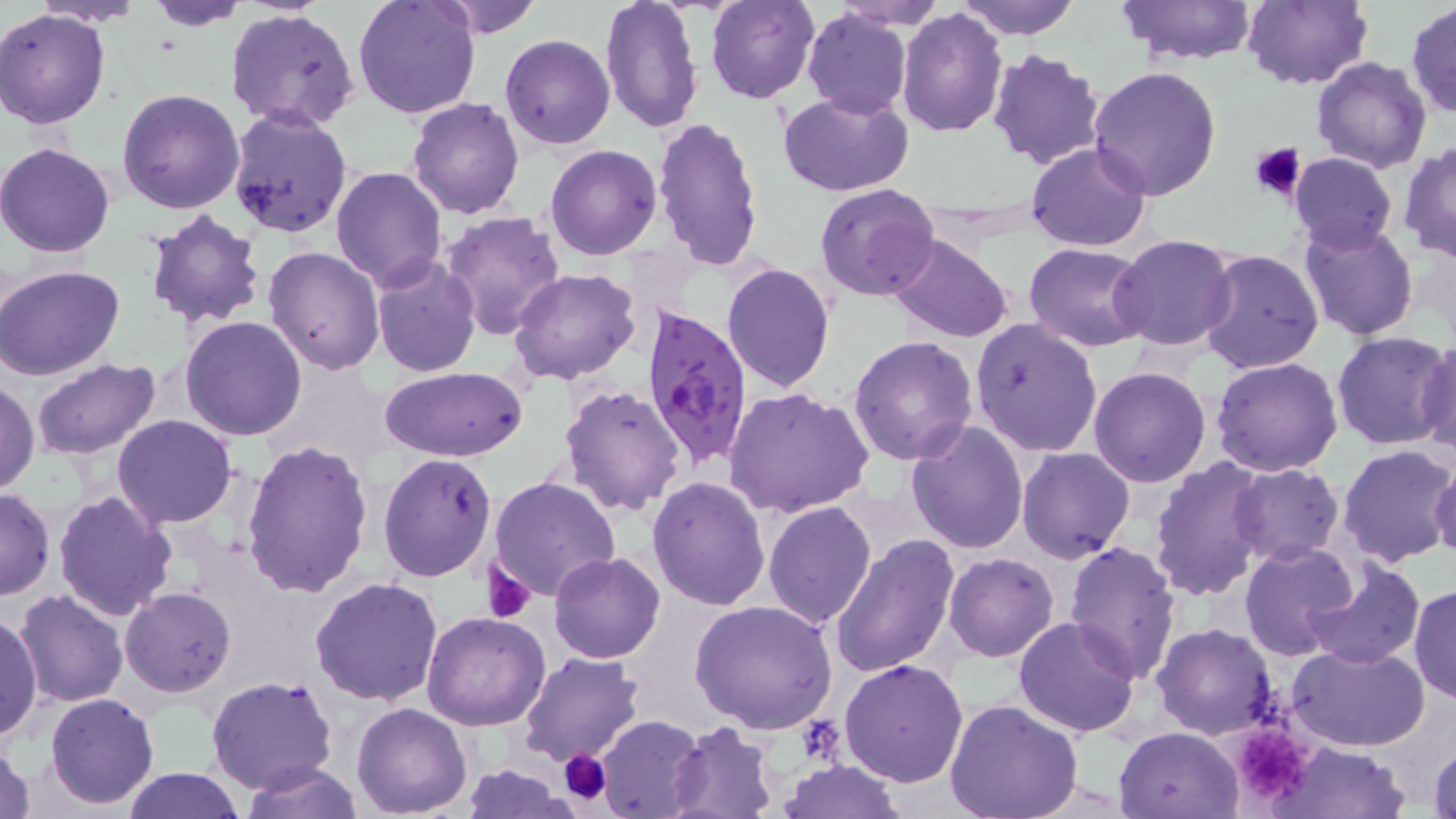

Summary:
  - Coordinate format: approximate bounding boxes as (x1,y1)-(x2,y2) corner pairs in pixels
  - Uninfected red blood cell locations: (140,0)-(250,29), (354,0)-(481,122), (431,0)-(543,40), (598,0)-(704,135), (705,0)-(819,104), (830,0)-(947,31), (953,0)-(1083,40), (1116,0)-(1260,66), (1240,0)-(1371,90), (31,2)-(148,27), (1406,3)-(1455,118), (227,7)-(361,133), (897,7)-(1009,137), (0,9)-(113,128), (802,9)-(913,119), (501,34)-(615,149), (988,49)-(1107,172), (1312,55)-(1431,173), (1087,64)-(1223,200), (779,87)-(916,199), (116,88)-(246,213), (408,98)-(525,220), (227,107)-(353,237), (651,116)-(763,271), (0,141)-(118,257), (1026,141)-(1152,250), (1400,142)-(1456,261), (545,145)-(663,261), (1288,153)-(1398,256), (331,166)-(447,290), (814,184)-(941,302), (143,210)-(267,331), (438,210)-(566,341), (1298,218)-(1420,340), (1110,233)-(1239,351), (888,235)-(1014,343), (1024,241)-(1150,351), (263,245)-(384,375), (1199,248)-(1324,375), (370,255)-(481,376), (722,262)-(836,394), (0,265)-(127,381), (509,269)-(641,385), (181,317)-(307,441), (970,318)-(1103,456), (1331,330)-(1455,449), (849,335)-(980,466), (1415,336)-(1456,459), (1212,357)-(1344,476), (32,359)-(161,458), (382,367)-(529,460), (1089,367)-(1212,487), (1,379)-(39,495), (558,383)-(689,517), (723,384)-(876,520), (113,414)-(237,529), (905,420)-(1031,555), (241,439)-(374,597), (1336,445)-(1456,568), (1017,447)-(1136,564), (377,453)-(497,582), (1148,456)-(1272,601), (1429,458)-(1456,564), (1228,464)-(1344,565), (647,476)-(772,611), (489,477)-(621,603), (0,488)-(54,600), (54,490)-(179,621), (762,499)-(878,629), (830,535)-(959,679), (1064,540)-(1183,683), (1240,541)-(1362,661), (549,551)-(665,663), (943,553)-(1059,662), (1302,555)-(1426,670), (309,575)-(446,707), (1410,582)-(1456,704), (121,587)-(235,696), (14,590)-(129,706), (0,598)-(80,726), (688,600)-(839,733), (1,609)-(44,744), (421,611)-(550,731), (1014,616)-(1142,737), (1152,622)-(1278,740), (1286,643)-(1432,749), (519,652)-(643,766), (839,660)-(970,788), (207,675)-(337,793), (45,692)-(160,808), (943,698)-(1085,819), (352,703)-(473,817), (595,714)-(706,819), (666,721)-(781,818), (1115,725)-(1243,817), (1,738)-(36,819), (1266,740)-(1410,819), (1427,740)-(1456,819), (776,759)-(907,817), (238,761)-(366,818), (459,764)-(570,818), (122,767)-(245,819)
  - Platelet locations: (1250,141)-(1307,201), (481,559)-(538,622), (1233,726)-(1312,796), (560,748)-(612,803)
  - Plasmodium falciparum-infected red blood cell locations: (641,306)-(757,466)
  - Slide-level diagnosis: Plasmodium falciparum
  - Modality: optical microscopy
  - Stain: May-Grünwald-Giemsa
  - Image size: 1456×819 pixels
  - Preparation: thin blood smear
  - Magnification: 1000x
  - Field of view: single